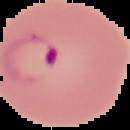

Summary:
  - Image size: 130×130 pixels
  - Result: malaria parasites detected
  - Image type: cell region segmented out of the field of view; surrounding area masked to black
  - Preparation: thin blood film